Assess this cell for malaria.
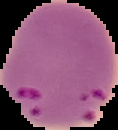
Parasitized.

preparation = thin blood film
image type = cell region segmented out of the field of view; surrounding area masked to black
image size = 118×130 pixels